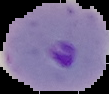 Image is 109×94 pixels. From a thin blood smear. The area outside the segmented cell region is set to black. Result: Plasmodium parasites detected.